State which parasite is depicted.
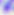

This is Toxoplasma gondii.

Micrograph. 400x magnification.